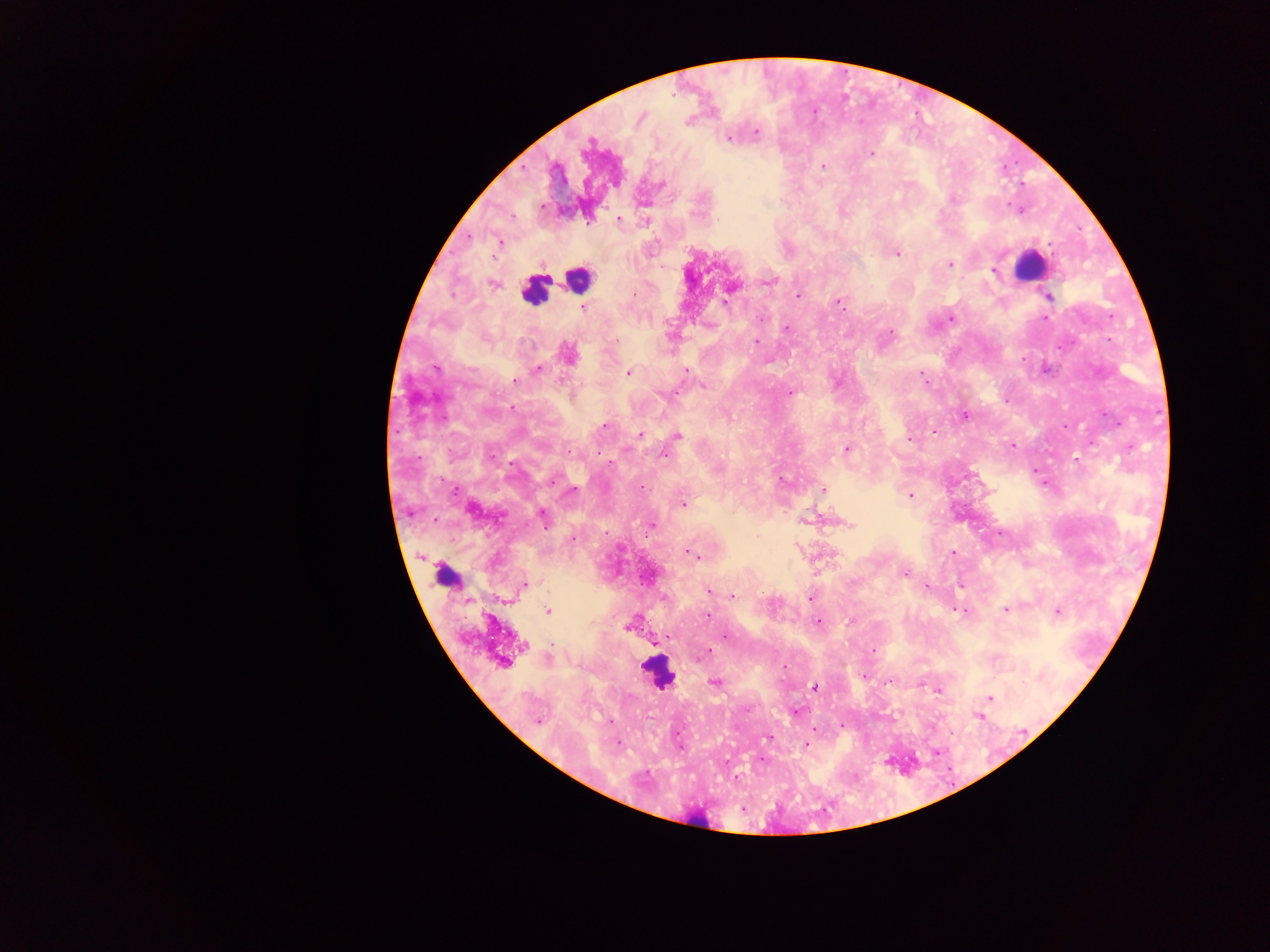
Approximate centers as {x, y} in pixels.
Summary:
  - Leukocyte locations: {1030, 265}, {578, 277}, {534, 290}, {450, 576}, {657, 673}
  - Malaria parasite locations: {640, 117}, {688, 120}, {755, 132}, {729, 137}, {871, 153}, {823, 166}, {661, 184}, {617, 218}, {468, 235}, {499, 241}, {896, 253}, {949, 264}, {994, 270}, {768, 280}, {492, 283}, {730, 287}, {797, 296}, {1048, 296}, {838, 301}, {583, 307}, {950, 318}, {1045, 318}, {786, 328}, {889, 333}, {757, 342}, {568, 354}, {537, 369}, {629, 372}, {921, 374}, {515, 381}, {789, 392}, {964, 415}, {605, 426}, {933, 432}, {639, 434}, {676, 436}, {909, 439}, {1012, 445}, {846, 448}, {664, 454}, {1076, 458}, {607, 463}, {1036, 471}, {552, 479}, {781, 479}, {640, 487}, {823, 489}, {910, 495}, {683, 503}, {471, 508}, {542, 516}, {803, 520}, {848, 524}, {650, 525}, {573, 537}, {953, 552}, {690, 554}, {904, 574}, {647, 576}, {961, 585}, {523, 586}, {926, 586}, {709, 591}, {732, 596}, {810, 597}, {957, 609}, {1005, 609}, {547, 611}, {1057, 611}, {708, 615}, {819, 621}, {630, 624}, {726, 635}, {667, 638}, {655, 641}, {873, 650}, {706, 653}, {503, 661}, {862, 676}, {890, 680}, {715, 682}, {814, 687}, {938, 689}, {990, 698}, {795, 711}, {978, 716}, {538, 720}, {841, 724}, {768, 737}, {616, 743}, {806, 744}, {937, 752}, {761, 759}
  - Capture: mobile-phone photograph through a microscope
  - Preparation: thick blood film
  - Country: Ghana
  - Field of view: single
  - Image size: 1270×952 pixels